Report the malaria status of this cell.
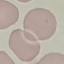
It is uninfected.

Cell patch, automatically extracted from a larger field of view and resized to 64 × 64 pixels. Photographed with a smartphone camera at the microscope eyepiece. Giemsa stain. Thin blood smear.